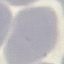
Summary:
  - Result: no malaria parasites detected
  - Capture: smartphone through the microscope eyepiece
  - Stain: Giemsa
  - Preparation: thin smear
  - Image type: automatically extracted cell patch, resized to 64 × 64 pixels